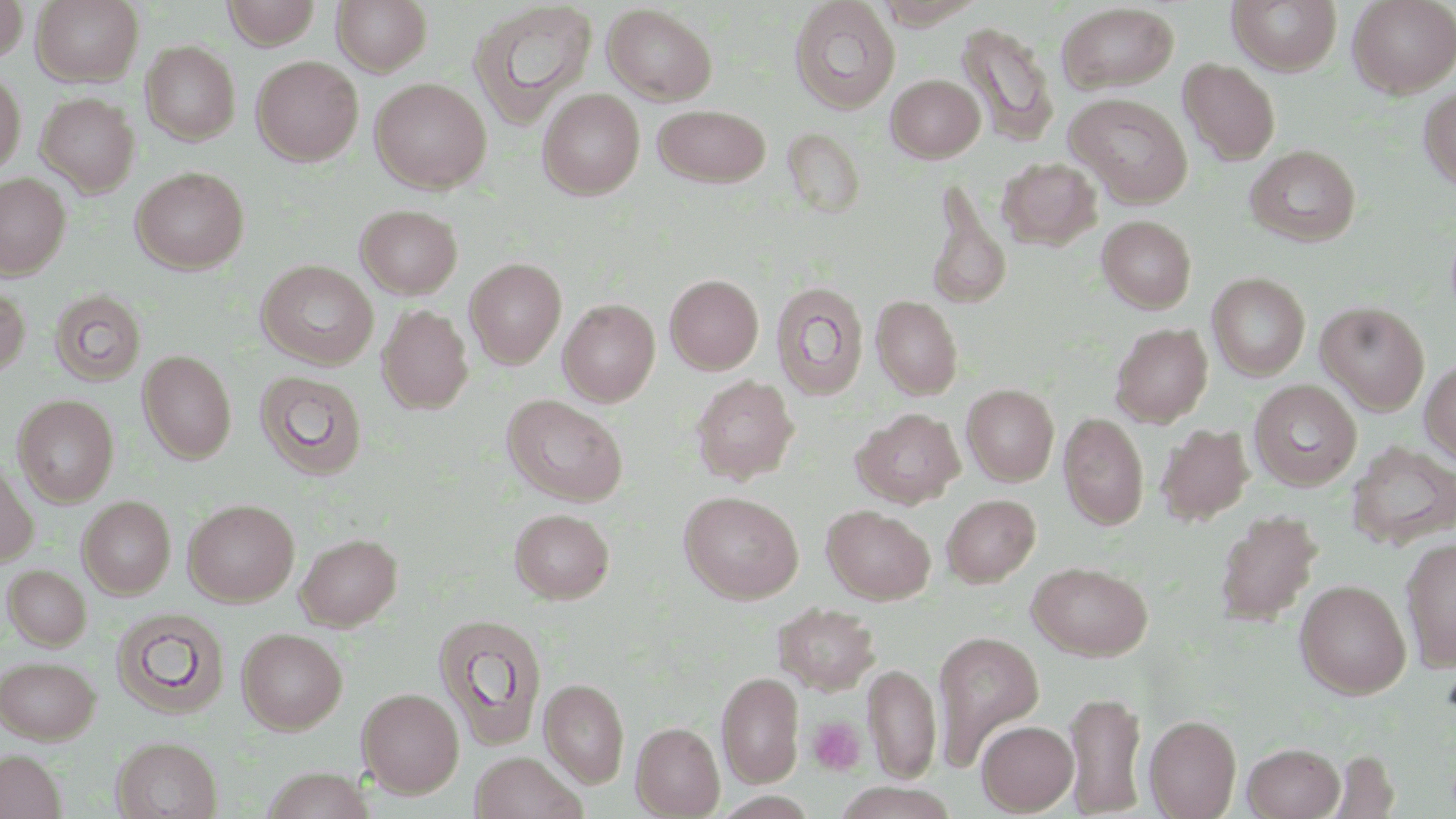

Approximate bounding boxes as named x1/y1/x2/y2 corners in pixels. Uninfected red blood cell locations: (x1=0, y1=0, x2=28, y2=63), (x1=32, y1=0, x2=143, y2=86), (x1=222, y1=0, x2=321, y2=48), (x1=332, y1=0, x2=432, y2=75), (x1=788, y1=0, x2=900, y2=114), (x1=874, y1=0, x2=985, y2=28), (x1=1227, y1=0, x2=1342, y2=75), (x1=1348, y1=0, x2=1456, y2=97), (x1=467, y1=2, x2=598, y2=129), (x1=1056, y1=2, x2=1180, y2=95), (x1=602, y1=4, x2=718, y2=105), (x1=956, y1=22, x2=1059, y2=146), (x1=140, y1=40, x2=240, y2=144), (x1=251, y1=56, x2=363, y2=166), (x1=1178, y1=57, x2=1281, y2=165), (x1=0, y1=70, x2=26, y2=176), (x1=886, y1=74, x2=985, y2=162), (x1=370, y1=78, x2=491, y2=192), (x1=1418, y1=87, x2=1456, y2=192), (x1=538, y1=89, x2=645, y2=199), (x1=36, y1=92, x2=139, y2=196), (x1=1065, y1=92, x2=1193, y2=207), (x1=652, y1=104, x2=771, y2=187), (x1=786, y1=136, x2=866, y2=220), (x1=1245, y1=145, x2=1362, y2=247), (x1=998, y1=158, x2=1102, y2=250), (x1=130, y1=166, x2=249, y2=274), (x1=0, y1=173, x2=71, y2=278), (x1=925, y1=181, x2=1012, y2=311), (x1=355, y1=204, x2=463, y2=299), (x1=1097, y1=215, x2=1196, y2=313), (x1=465, y1=258, x2=566, y2=369), (x1=256, y1=260, x2=379, y2=369), (x1=1207, y1=273, x2=1310, y2=380), (x1=665, y1=274, x2=764, y2=374), (x1=771, y1=281, x2=869, y2=401), (x1=0, y1=282, x2=31, y2=380), (x1=48, y1=289, x2=147, y2=386), (x1=871, y1=295, x2=963, y2=399), (x1=559, y1=299, x2=660, y2=406), (x1=1316, y1=301, x2=1430, y2=414), (x1=377, y1=304, x2=474, y2=414), (x1=1110, y1=323, x2=1214, y2=427), (x1=138, y1=349, x2=237, y2=463), (x1=1419, y1=359, x2=1456, y2=466), (x1=254, y1=369, x2=368, y2=480), (x1=690, y1=375, x2=799, y2=484), (x1=1249, y1=379, x2=1362, y2=491), (x1=961, y1=384, x2=1059, y2=485), (x1=12, y1=394, x2=119, y2=506), (x1=502, y1=394, x2=628, y2=505), (x1=852, y1=408, x2=965, y2=508), (x1=1059, y1=412, x2=1148, y2=530), (x1=1156, y1=423, x2=1254, y2=525), (x1=1346, y1=441, x2=1456, y2=549), (x1=0, y1=458, x2=38, y2=567), (x1=679, y1=491, x2=803, y2=603), (x1=942, y1=494, x2=1040, y2=587), (x1=77, y1=495, x2=176, y2=598), (x1=183, y1=498, x2=299, y2=606), (x1=822, y1=505, x2=935, y2=604), (x1=510, y1=508, x2=614, y2=603), (x1=1213, y1=510, x2=1323, y2=627), (x1=295, y1=533, x2=402, y2=630), (x1=1400, y1=537, x2=1456, y2=672), (x1=1027, y1=561, x2=1153, y2=660), (x1=3, y1=565, x2=92, y2=650), (x1=1295, y1=579, x2=1412, y2=699), (x1=773, y1=602, x2=880, y2=694), (x1=110, y1=607, x2=230, y2=718), (x1=433, y1=613, x2=547, y2=749), (x1=236, y1=627, x2=347, y2=733), (x1=932, y1=631, x2=1044, y2=767), (x1=0, y1=655, x2=100, y2=743), (x1=863, y1=663, x2=941, y2=781), (x1=717, y1=671, x2=803, y2=786), (x1=540, y1=678, x2=629, y2=787), (x1=357, y1=687, x2=465, y2=797), (x1=1065, y1=690, x2=1147, y2=816), (x1=1145, y1=714, x2=1241, y2=818), (x1=977, y1=720, x2=1078, y2=815), (x1=632, y1=722, x2=725, y2=818), (x1=113, y1=736, x2=222, y2=819), (x1=1242, y1=742, x2=1345, y2=818), (x1=0, y1=749, x2=65, y2=818), (x1=469, y1=750, x2=587, y2=819), (x1=832, y1=782, x2=960, y2=819). Platelet locations: (x1=809, y1=717, x2=866, y2=775). Slide-level diagnosis: negative for blood parasites. May-Grünwald-Giemsa stain. One field of a larger specimen. Thin blood film. Captured at 1000x magnification. Optical microscopy. Image is 1456×819 pixels.